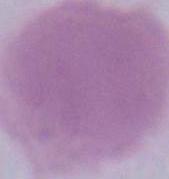

Summary:
  - Identification: erythrocyte
  - Magnification: 1000x
  - Modality: micrograph